Identify the parasite.
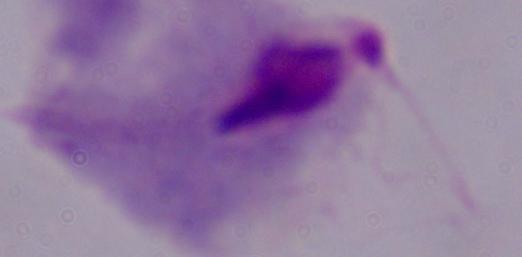
This is a trichomonad.

magnification: 1000x
modality: micrograph